Report the malaria status of this cell.
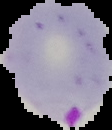

It is parasitized.

From a thin blood film. Cell region segmented out of the field of view; the surrounding area is masked to black. Image is 112×130 pixels.